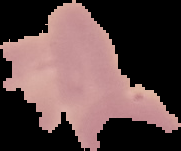

result = no malaria parasites seen
image type = segmented cell region on a black background
preparation = thin blood smear
image size = 181×151 pixels